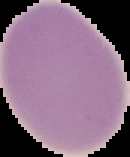 Segmented cell region on a black background. Image is 130×157 pixels. From a thin blood smear. Malaria status: uninfected.